Identify the cell.
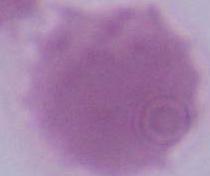
This is an erythrocyte.

Summary:
  - Magnification: 1000x
  - Modality: photomicrograph